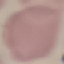
malaria status = uninfected
capture = smartphone through the microscope eyepiece
preparation = thin blood film
stain = Giemsa
image type = cell patch, automatically extracted from a larger field of view and resized to 64 × 64 pixels